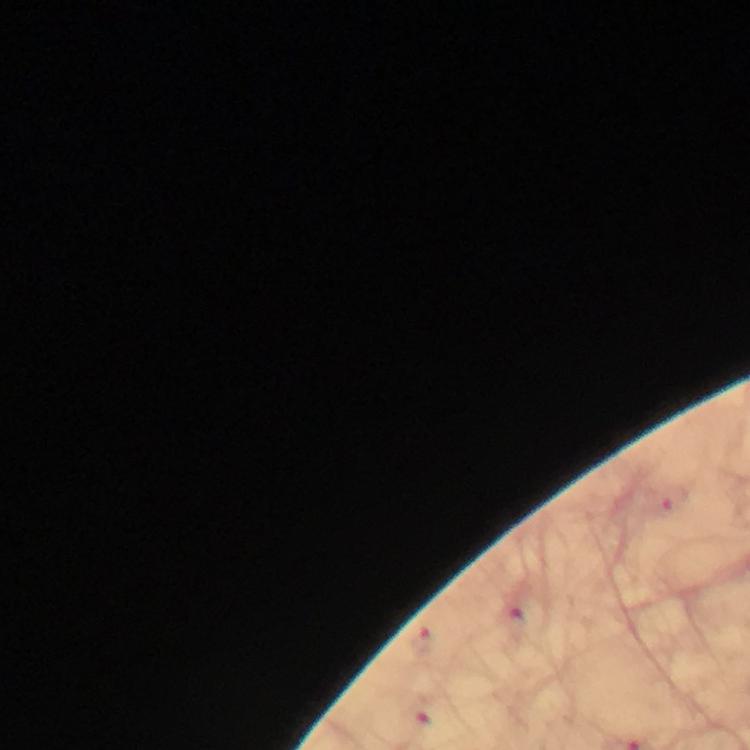 Approximate centers as (x, y) in pixels. Plasmodium parasite locations: (518, 623). Thick smear. Immersion oil applied. Image is 750×750 pixels. From a diagnostic examination for malaria. Smartphone photograph taken through a microscope. Giemsa stain. A crop from one field of view. 100x magnification.